Classify this cell by malaria status.
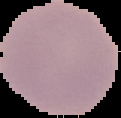

It is uninfected.

image type = segmented cell region on a black background
image size = 121×118 pixels
preparation = thin blood smear